State the blood parasite species.
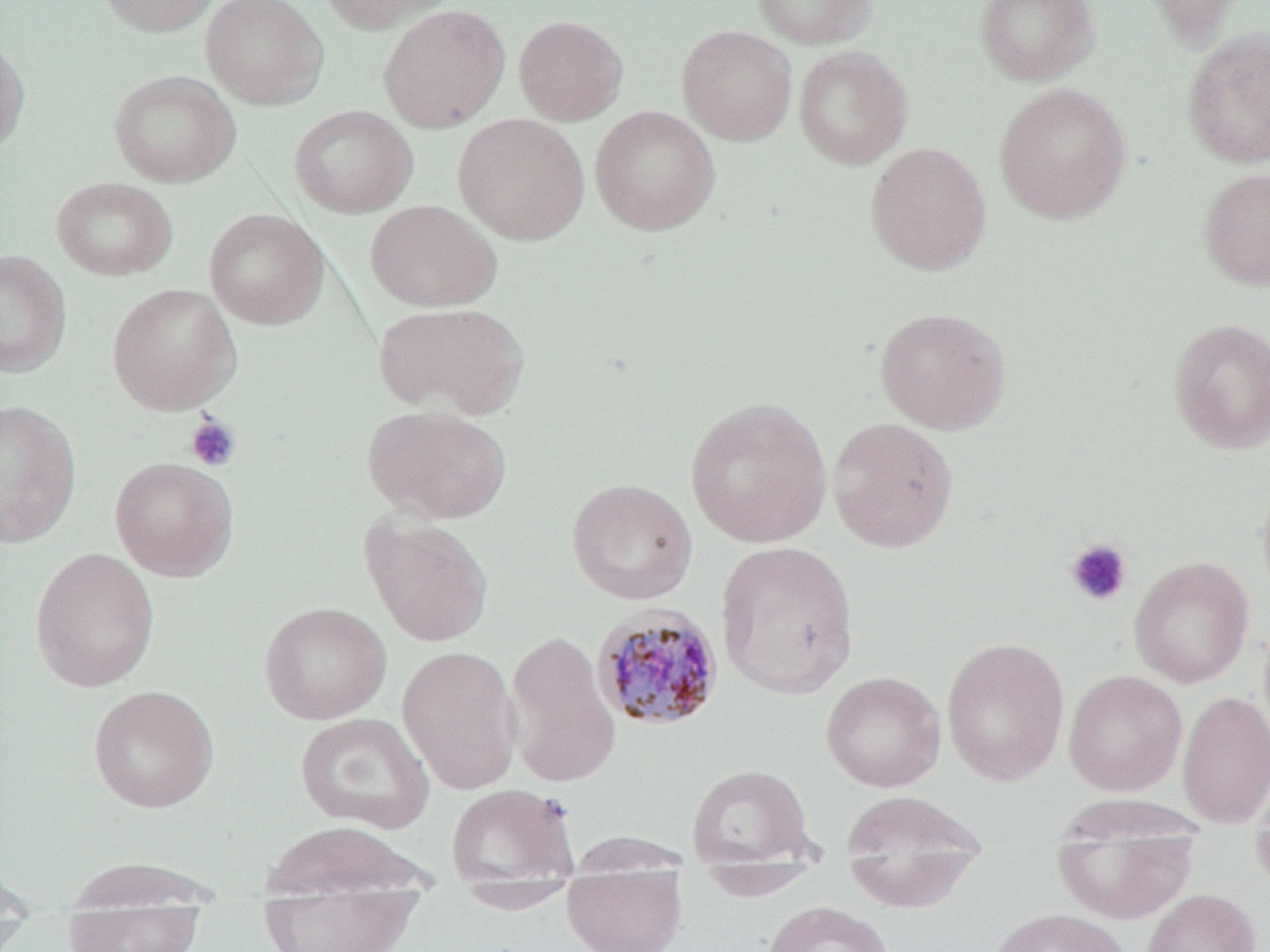
Plasmodium malariae.

Summary:
  - Coordinate format: approximate bounding boxes as named x1/y1/x2/y2 corners in pixels
  - Platelet locations: (x1=185, y1=413, x2=241, y2=473), (x1=1065, y1=538, x2=1132, y2=607)
  - Plasmodium malariae-infected red blood cell locations: (x1=591, y1=604, x2=726, y2=731)
  - Uninfected red blood cell locations: (x1=96, y1=0, x2=223, y2=36), (x1=201, y1=0, x2=329, y2=109), (x1=316, y1=0, x2=460, y2=32), (x1=751, y1=0, x2=875, y2=49), (x1=974, y1=0, x2=1099, y2=86), (x1=1140, y1=0, x2=1249, y2=49), (x1=378, y1=4, x2=510, y2=132), (x1=514, y1=15, x2=628, y2=125), (x1=676, y1=25, x2=797, y2=145), (x1=1182, y1=28, x2=1270, y2=168), (x1=0, y1=33, x2=30, y2=155), (x1=793, y1=46, x2=913, y2=170), (x1=108, y1=70, x2=240, y2=187), (x1=994, y1=82, x2=1132, y2=225), (x1=288, y1=105, x2=418, y2=218), (x1=590, y1=105, x2=720, y2=235), (x1=452, y1=113, x2=590, y2=245), (x1=865, y1=141, x2=991, y2=275), (x1=1198, y1=166, x2=1270, y2=291), (x1=51, y1=176, x2=177, y2=281), (x1=366, y1=199, x2=502, y2=312), (x1=204, y1=208, x2=328, y2=329), (x1=0, y1=250, x2=71, y2=377), (x1=107, y1=283, x2=241, y2=414), (x1=375, y1=302, x2=529, y2=419), (x1=874, y1=306, x2=1012, y2=434), (x1=1167, y1=317, x2=1270, y2=455), (x1=685, y1=396, x2=833, y2=547), (x1=0, y1=399, x2=81, y2=549), (x1=362, y1=405, x2=512, y2=524), (x1=827, y1=417, x2=959, y2=553), (x1=110, y1=456, x2=238, y2=581), (x1=1256, y1=475, x2=1270, y2=606), (x1=566, y1=477, x2=699, y2=605), (x1=360, y1=513, x2=494, y2=647), (x1=715, y1=540, x2=860, y2=700), (x1=30, y1=547, x2=159, y2=692), (x1=1128, y1=556, x2=1255, y2=687), (x1=259, y1=601, x2=391, y2=724), (x1=503, y1=629, x2=621, y2=789), (x1=940, y1=636, x2=1070, y2=786), (x1=397, y1=644, x2=522, y2=795), (x1=1063, y1=669, x2=1188, y2=795), (x1=821, y1=670, x2=946, y2=792), (x1=88, y1=685, x2=219, y2=812), (x1=1177, y1=690, x2=1270, y2=828), (x1=295, y1=712, x2=434, y2=834), (x1=686, y1=763, x2=816, y2=868), (x1=1248, y1=778, x2=1270, y2=893), (x1=446, y1=783, x2=581, y2=888), (x1=840, y1=790, x2=988, y2=912), (x1=259, y1=820, x2=437, y2=903), (x1=1050, y1=825, x2=1200, y2=924), (x1=60, y1=856, x2=227, y2=909), (x1=562, y1=863, x2=688, y2=952), (x1=695, y1=865, x2=824, y2=901), (x1=454, y1=880, x2=582, y2=914), (x1=256, y1=886, x2=427, y2=952), (x1=1141, y1=889, x2=1261, y2=952), (x1=761, y1=900, x2=895, y2=952), (x1=987, y1=907, x2=1133, y2=952), (x1=63, y1=908, x2=205, y2=952)
  - Magnification: 1000x
  - Field of view: one of a larger specimen
  - Image size: 1270×952 pixels
  - Preparation: thin blood smear
  - Stain: May-Grünwald-Giemsa
  - Modality: optical microscopy